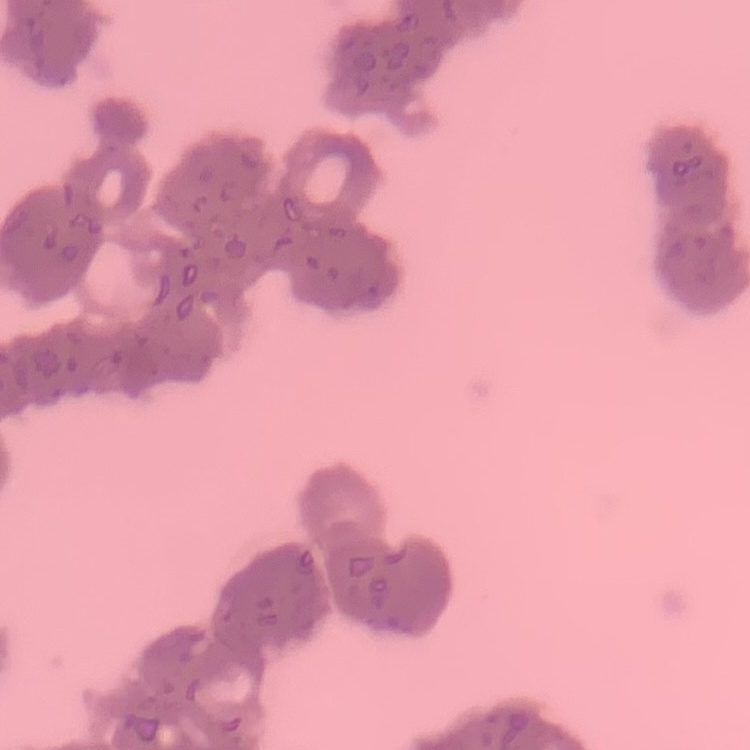

Summary:
  - Red blood cell morphology: rouleaux formation
  - Preparation: thin blood film
  - Stain: Field's or Giemsa
  - Image type: square crop of a larger photomicrograph